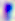 400x magnification. Photomicrograph. Toxoplasma gondii is shown.